Comment on the morphology of the red blood cells.
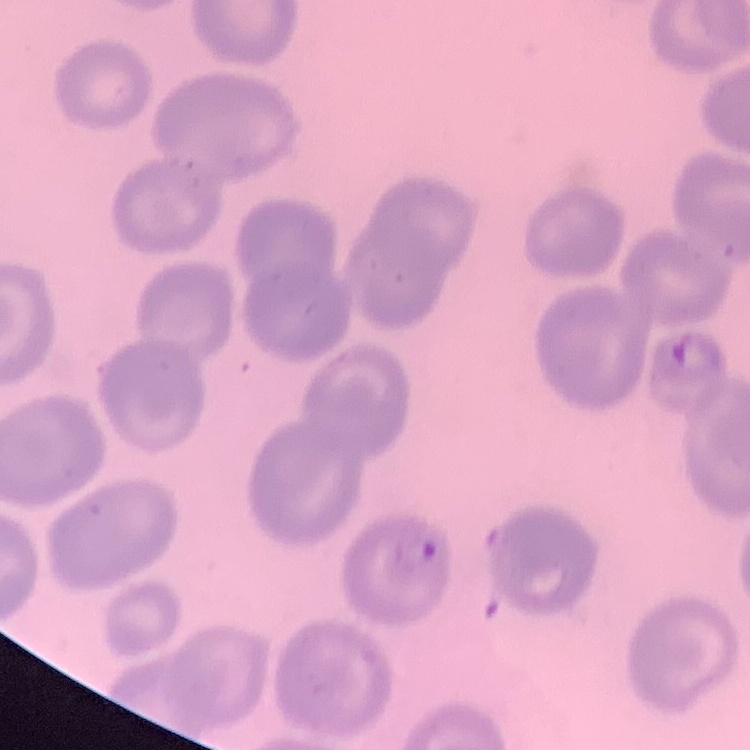
No rouleaux formation.

Thin blood smear. Field's or Giemsa stain. Square crop of a larger photomicrograph.